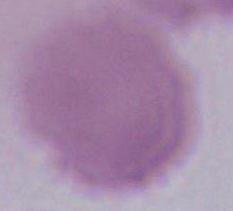

Summary:
  - Magnification: 1000x
  - Identification: red blood cell
  - Modality: photomicrograph